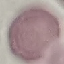

malaria status = uninfected
preparation = thin blood film
capture = smartphone through the microscope eyepiece
stain = Giemsa
image type = cell patch, automatically extracted from a larger field of view and resized to 64 × 64 pixels